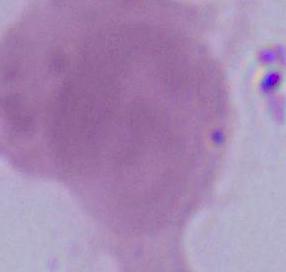

Summary:
  - Identification: erythrocyte
  - Modality: micrograph
  - Magnification: 1000x